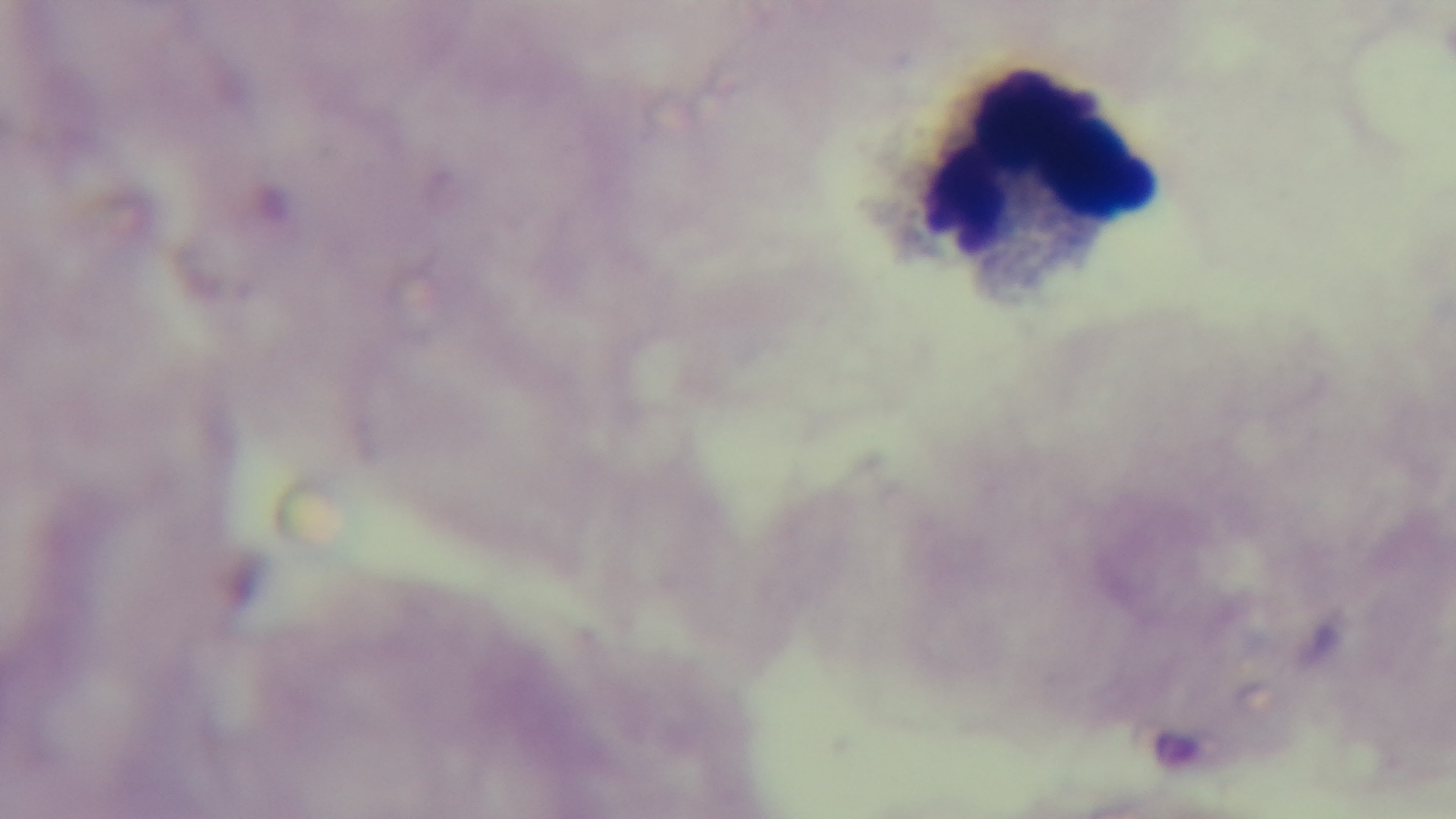

Summary:
  - Modality: light microscopy
  - Objective: 100x oil immersion
  - Preparation: thick smear
  - Malaria status: negative
  - Capture: mounted 4K digital camera
  - Stain: Giemsa
  - Field of view: one from the slide